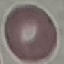 Malaria status: uninfected. Automatically extracted cell patch, resized to 64 × 64 pixels. Acquired by smartphone through the microscope eyepiece. Thin smear of blood. Giemsa stain.